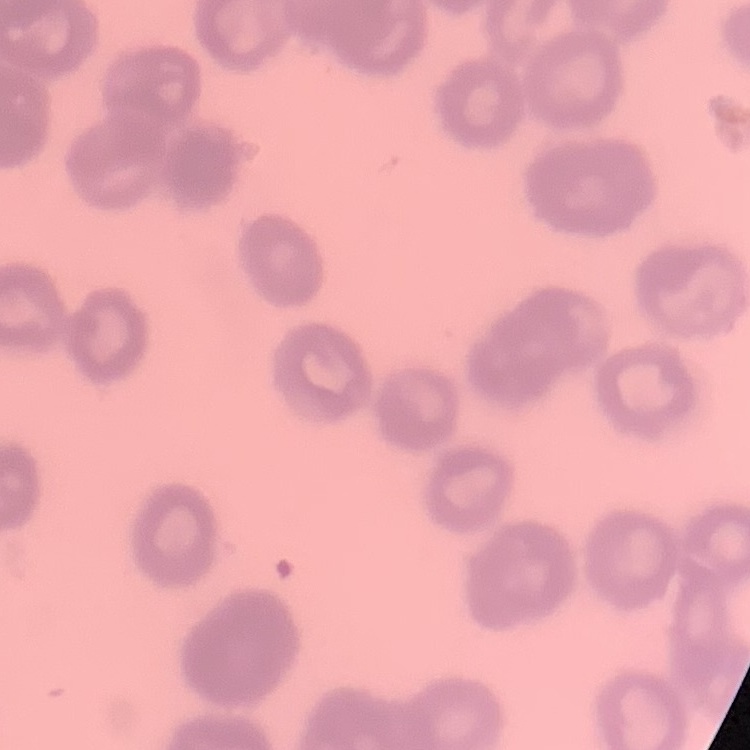
{
  "erythrocyte_morphology": "rouleaux formation",
  "stain": "Field's or Giemsa",
  "preparation": "thin blood film",
  "image_type": "square crop of a larger photomicrograph"
}